Identify the blood parasite species.
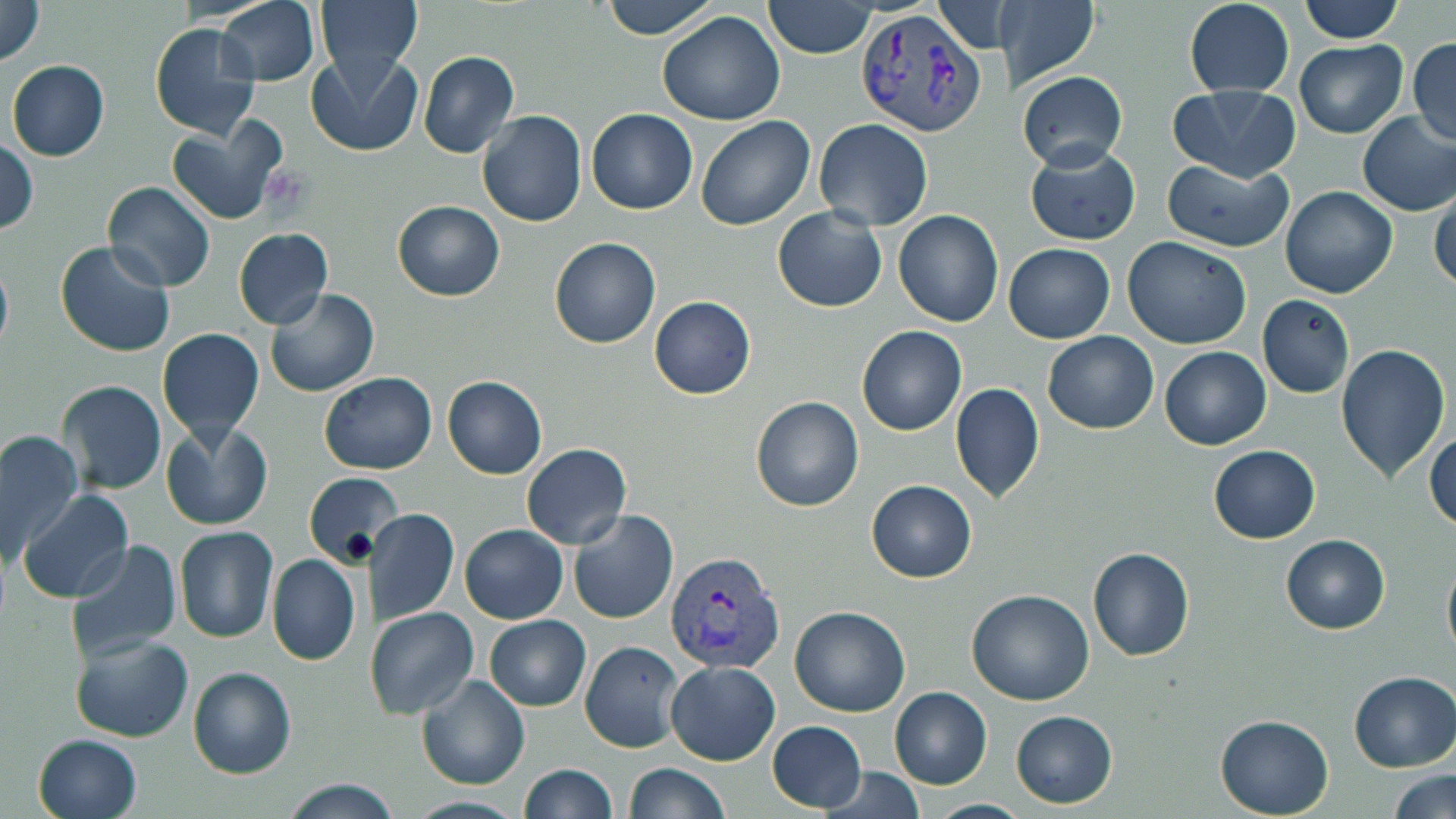
Plasmodium vivax.

Approximate bounding boxes as named x1/y1/x2/y2 corners in pixels. Plasmodium vivax-infected red blood cell locations: (x1=851, y1=5, x2=984, y2=135), (x1=664, y1=551, x2=787, y2=675). Platelet locations: (x1=261, y1=165, x2=315, y2=220). Uninfected red blood cell locations: (x1=0, y1=0, x2=47, y2=67), (x1=317, y1=0, x2=421, y2=79), (x1=601, y1=0, x2=716, y2=40), (x1=762, y1=0, x2=878, y2=58), (x1=998, y1=0, x2=1099, y2=95), (x1=1297, y1=0, x2=1403, y2=44), (x1=933, y1=1, x2=1005, y2=55), (x1=1185, y1=1, x2=1293, y2=96), (x1=218, y1=2, x2=318, y2=84), (x1=657, y1=11, x2=786, y2=126), (x1=149, y1=22, x2=262, y2=139), (x1=1407, y1=38, x2=1456, y2=146), (x1=1295, y1=40, x2=1407, y2=137), (x1=307, y1=49, x2=422, y2=157), (x1=419, y1=51, x2=520, y2=160), (x1=6, y1=60, x2=110, y2=161), (x1=1019, y1=71, x2=1126, y2=170), (x1=1167, y1=85, x2=1302, y2=184), (x1=586, y1=109, x2=697, y2=214), (x1=478, y1=111, x2=587, y2=227), (x1=1356, y1=112, x2=1456, y2=215), (x1=696, y1=116, x2=816, y2=232), (x1=168, y1=117, x2=285, y2=224), (x1=814, y1=118, x2=933, y2=232), (x1=0, y1=138, x2=37, y2=235), (x1=1025, y1=141, x2=1140, y2=246), (x1=1160, y1=158, x2=1294, y2=253), (x1=101, y1=181, x2=216, y2=293), (x1=1280, y1=185, x2=1398, y2=298), (x1=1430, y1=188, x2=1456, y2=295), (x1=393, y1=200, x2=505, y2=301), (x1=771, y1=206, x2=887, y2=313), (x1=80, y1=209, x2=208, y2=338), (x1=895, y1=209, x2=1004, y2=327), (x1=232, y1=228, x2=334, y2=330), (x1=1123, y1=235, x2=1253, y2=349), (x1=549, y1=237, x2=661, y2=349), (x1=55, y1=239, x2=177, y2=357), (x1=1003, y1=244, x2=1115, y2=344), (x1=0, y1=253, x2=13, y2=359), (x1=264, y1=287, x2=380, y2=398), (x1=1257, y1=294, x2=1355, y2=398), (x1=650, y1=295, x2=757, y2=399), (x1=857, y1=325, x2=966, y2=436), (x1=157, y1=327, x2=266, y2=441), (x1=1042, y1=330, x2=1159, y2=435), (x1=1336, y1=344, x2=1451, y2=484), (x1=1159, y1=346, x2=1271, y2=450), (x1=318, y1=373, x2=437, y2=473), (x1=442, y1=375, x2=547, y2=480), (x1=57, y1=381, x2=167, y2=496), (x1=950, y1=382, x2=1044, y2=504), (x1=750, y1=395, x2=865, y2=512), (x1=160, y1=419, x2=272, y2=533), (x1=1426, y1=429, x2=1456, y2=531), (x1=0, y1=431, x2=85, y2=562), (x1=521, y1=443, x2=632, y2=549), (x1=1208, y1=445, x2=1322, y2=544), (x1=304, y1=473, x2=400, y2=568), (x1=865, y1=481, x2=978, y2=582), (x1=17, y1=491, x2=134, y2=605), (x1=368, y1=507, x2=459, y2=626), (x1=569, y1=510, x2=678, y2=624), (x1=460, y1=524, x2=568, y2=624), (x1=175, y1=525, x2=277, y2=643), (x1=1281, y1=533, x2=1390, y2=636), (x1=63, y1=540, x2=182, y2=663), (x1=1087, y1=548, x2=1195, y2=662), (x1=1441, y1=552, x2=1456, y2=666), (x1=267, y1=553, x2=361, y2=667), (x1=966, y1=589, x2=1094, y2=706), (x1=788, y1=605, x2=911, y2=716), (x1=366, y1=606, x2=479, y2=720), (x1=483, y1=614, x2=591, y2=711), (x1=68, y1=633, x2=193, y2=742), (x1=579, y1=640, x2=682, y2=753), (x1=665, y1=662, x2=780, y2=765), (x1=187, y1=666, x2=296, y2=779), (x1=1349, y1=670, x2=1456, y2=771), (x1=417, y1=675, x2=530, y2=790), (x1=889, y1=687, x2=992, y2=790), (x1=1011, y1=710, x2=1117, y2=808), (x1=1214, y1=715, x2=1334, y2=817), (x1=766, y1=722, x2=867, y2=813), (x1=33, y1=733, x2=142, y2=819), (x1=518, y1=763, x2=616, y2=819), (x1=622, y1=763, x2=730, y2=819), (x1=822, y1=766, x2=925, y2=819), (x1=1386, y1=769, x2=1456, y2=819), (x1=280, y1=779, x2=400, y2=817), (x1=925, y1=799, x2=1030, y2=817). May-Grünwald-Giemsa-stained preparation. Image is 1456×819 pixels. 1000x magnification. Light microscopy. Thin blood smear. One field of a larger specimen.